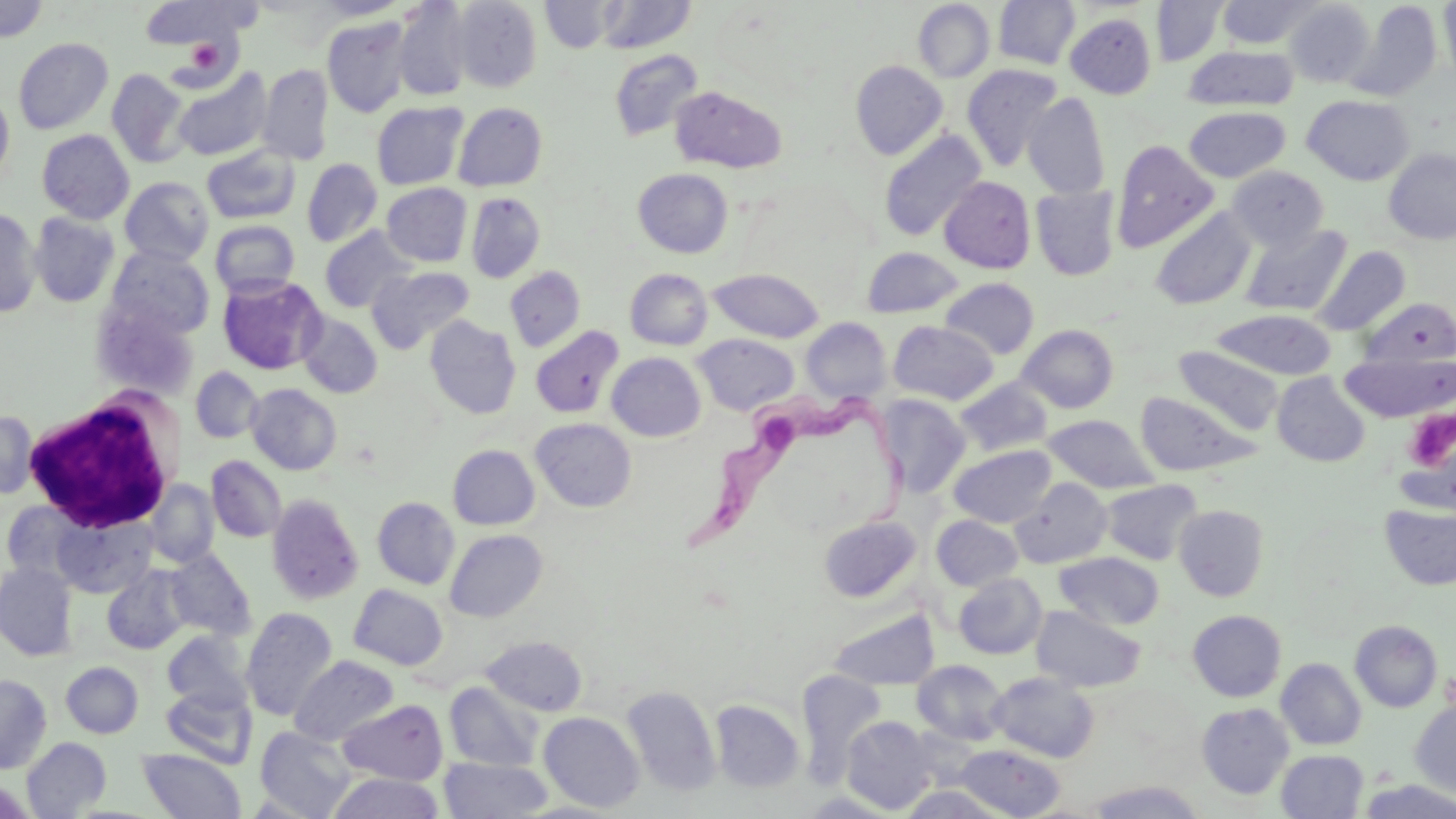

Approximate bounding boxes as (x1,y1)-(x2,y2) corner pairs in pixels. White blood cell locations: (22,392)-(182,534). Trypanosoma brucei locations: (680,379)-(916,558). Uninfected red blood cell locations: (313,0)-(412,20), (452,0)-(542,93), (596,0)-(696,54), (993,0)-(1080,70), (1216,0)-(1322,49), (1284,0)-(1375,88), (1439,0)-(1456,86), (0,1)-(50,42), (392,1)-(474,101), (541,1)-(620,52), (912,1)-(995,83), (1151,1)-(1228,66), (138,2)-(252,50), (1344,2)-(1443,101), (1065,13)-(1157,98), (322,16)-(412,118), (13,38)-(113,134), (1182,45)-(1299,111), (609,49)-(704,142), (850,60)-(948,160), (258,64)-(334,166), (961,64)-(1063,171), (172,67)-(273,162), (106,68)-(189,167), (670,86)-(787,174), (0,89)-(15,188), (1023,92)-(1110,199), (1302,95)-(1414,185), (372,101)-(468,190), (453,102)-(547,191), (1184,106)-(1290,183), (878,128)-(987,242), (36,129)-(135,224), (1110,140)-(1219,253), (201,146)-(300,224), (1383,148)-(1456,244), (302,158)-(382,247), (1227,166)-(1328,251), (633,168)-(733,258), (120,176)-(214,266), (939,176)-(1036,274), (382,183)-(472,267), (1030,185)-(1121,281), (466,192)-(545,283), (1150,207)-(1256,311), (0,208)-(41,317), (28,212)-(120,307), (210,220)-(300,298), (1240,224)-(1351,317), (319,226)-(415,313), (105,246)-(215,340), (1313,246)-(1411,335), (861,247)-(964,318), (368,265)-(474,353), (505,266)-(585,352), (625,268)-(712,350), (709,269)-(824,343), (218,275)-(327,374), (940,278)-(1039,360), (1359,297)-(1456,369), (95,300)-(197,402), (1211,309)-(1337,380), (299,312)-(383,398), (424,316)-(521,419), (801,317)-(892,403), (888,321)-(999,405), (1017,324)-(1119,413), (530,326)-(623,418), (693,334)-(799,416), (1173,346)-(1284,436), (1339,351)-(1455,423), (607,352)-(705,441), (190,367)-(264,444), (1272,372)-(1370,466), (955,378)-(1052,457), (246,383)-(342,475), (1135,391)-(1255,477), (875,394)-(970,496), (0,410)-(39,499), (1042,414)-(1160,494), (530,418)-(636,512), (448,444)-(540,529), (949,444)-(1057,527), (206,456)-(286,542), (1011,477)-(1112,568), (1100,479)-(1202,565), (146,480)-(219,568), (267,494)-(364,604), (372,497)-(460,589), (1,501)-(85,583), (1380,503)-(1456,590), (1174,504)-(1269,601), (50,510)-(157,599), (931,515)-(1024,591), (818,516)-(920,602), (445,529)-(547,622), (164,548)-(256,640), (1054,551)-(1164,630), (0,562)-(78,661), (102,567)-(190,655), (953,573)-(1047,659), (348,584)-(448,670), (1031,605)-(1145,692), (241,607)-(338,721), (829,608)-(939,690), (1187,610)-(1286,701), (1350,620)-(1443,712), (162,631)-(253,712), (483,636)-(587,716), (290,656)-(399,746), (1276,658)-(1366,750), (912,660)-(1009,745), (60,662)-(143,738), (796,669)-(887,786), (988,671)-(1099,762), (0,674)-(52,773), (444,682)-(542,771), (160,685)-(257,768), (621,685)-(721,796), (338,699)-(448,784), (709,699)-(804,793), (1410,701)-(1456,798), (1197,703)-(1294,799), (539,712)-(644,812), (841,715)-(939,814), (255,726)-(356,818), (21,737)-(112,818), (955,744)-(1065,818), (138,748)-(246,818), (1276,750)-(1368,818), (439,757)-(552,818), (327,772)-(444,819), (1359,779)-(1456,819), (1087,780)-(1206,819), (897,785)-(1011,819). Platelet locations: (184,39)-(224,75), (1402,408)-(1455,487). Slide-level diagnosis: Trypanosoma brucei. May-Grünwald-Giemsa-stained preparation. Single field of view. Thin blood smear. Captured at 1000x magnification. Image is 1456×819 pixels. Light microscopy.